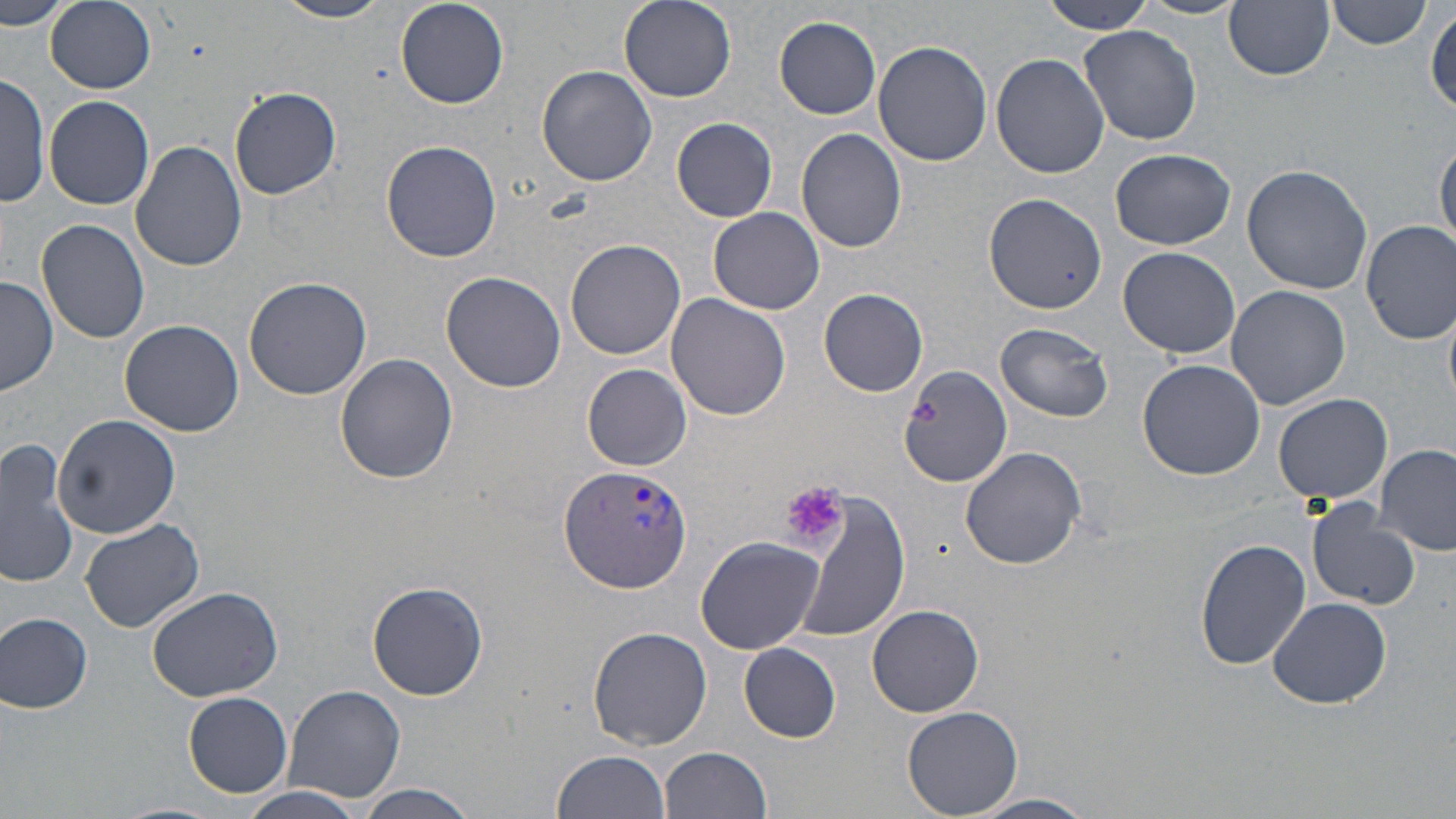

Summary:
  - Coordinate format: approximate bounding boxes as [x1, y1, x2, y2] in pixels
  - Uninfected red blood cell locations: [0, 0, 75, 32], [273, 0, 394, 23], [619, 0, 737, 102], [1045, 0, 1157, 35], [1132, 0, 1249, 20], [1328, 0, 1431, 49], [47, 1, 158, 93], [394, 1, 509, 109], [1224, 1, 1336, 81], [1427, 7, 1456, 114], [774, 16, 881, 120], [1077, 24, 1202, 145], [873, 39, 993, 167], [990, 53, 1109, 178], [536, 64, 657, 187], [0, 74, 50, 207], [230, 87, 342, 200], [44, 95, 155, 210], [673, 117, 778, 221], [796, 128, 907, 253], [130, 139, 249, 270], [381, 140, 503, 262], [1435, 140, 1456, 253], [1110, 148, 1235, 250], [1242, 163, 1373, 295], [986, 193, 1105, 314], [707, 207, 824, 315], [37, 218, 150, 344], [1361, 220, 1456, 345], [564, 239, 686, 360], [1118, 247, 1241, 357], [440, 270, 567, 393], [244, 275, 371, 399], [0, 276, 57, 396], [1226, 284, 1349, 409], [819, 289, 928, 397], [667, 296, 791, 421], [119, 318, 245, 437], [995, 322, 1116, 419], [334, 353, 458, 484], [1137, 358, 1267, 481], [583, 364, 692, 470], [897, 366, 1013, 488], [1273, 393, 1393, 504], [53, 413, 180, 537], [0, 438, 78, 591], [1377, 442, 1456, 557], [960, 446, 1087, 570], [793, 495, 912, 642], [1306, 498, 1421, 610], [79, 517, 204, 632], [695, 535, 826, 655], [1196, 537, 1311, 670], [367, 581, 488, 701], [145, 583, 284, 702], [1267, 596, 1392, 710], [867, 605, 984, 717], [1, 612, 95, 713], [588, 626, 712, 750], [739, 642, 842, 742], [282, 684, 408, 804], [184, 690, 294, 798], [901, 705, 1024, 819], [660, 747, 773, 819], [552, 749, 671, 819], [350, 784, 483, 818], [234, 788, 372, 819], [969, 794, 1099, 819]
  - Plasmodium vivax-infected red blood cell locations: [559, 465, 696, 593]
  - Platelet locations: [908, 397, 940, 429], [782, 480, 848, 550]
  - Slide-level diagnosis: Plasmodium vivax
  - Stain: May-Grünwald-Giemsa
  - Magnification: 1000x
  - Field of view: one of a larger specimen
  - Preparation: thin blood film
  - Image size: 1456×819 pixels
  - Modality: light microscopy